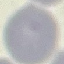
Malaria status: uninfected. Cell patch, automatically extracted from a larger field of view and resized to 64 × 64 pixels. Giemsa stain. Thin smear of blood. Acquired by smartphone through the microscope eyepiece.